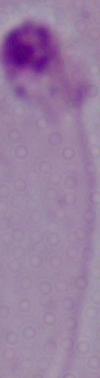
1000x magnification. Photomicrograph. A Leishmania parasite is seen.